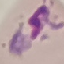
Result: malaria parasites detected. Giemsa-stained preparation. Automatically extracted cell patch, resized to 64 × 64 pixels. Thin blood film. Photographed with a smartphone camera at the microscope eyepiece.